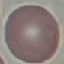
malaria status = uninfected
image type = automatically extracted cell patch, resized to 64 × 64 pixels
preparation = thin blood film
stain = Giemsa
capture = smartphone camera at the microscope eyepiece